Draw a bounding box around every parasitised red blood cell.
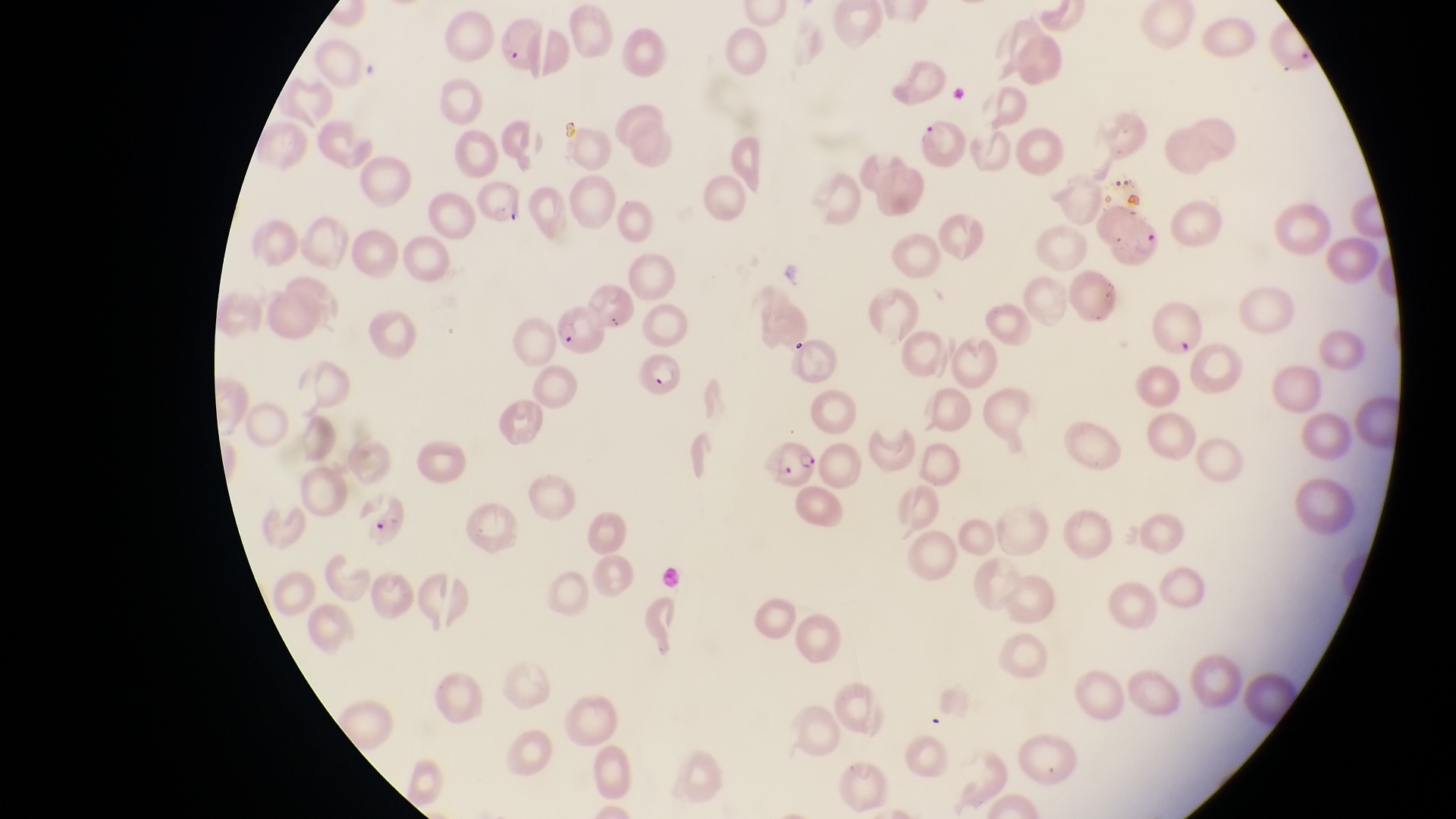
Approximate bounding boxes as [left, top, right, bottom] in pixels.
Parasitised red blood cells: [1099, 206, 1172, 261], [554, 306, 607, 356], [635, 353, 690, 399], [770, 435, 826, 491].

country: Uganda
magnification: 1000x
capture: smartphone photograph through the eyepiece of an Olympus CX-23 microscope
field_of_view: single
image_size: 1456×819 pixels
preparation: thin blood smear